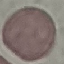
result: no malaria parasites seen
image_type: cell patch, automatically extracted from a larger field of view and resized to 64 × 64 pixels
preparation: thin smear
capture: smartphone camera at the microscope eyepiece
stain: Giemsa